Assess this cell for malaria.
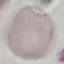

It is uninfected.

Thin blood film. Automatically extracted cell patch, resized to 64 × 64 pixels. Acquired by smartphone through the microscope eyepiece. Giemsa-stained preparation.